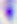
Micrograph. 400x magnification. Toxoplasma gondii is shown.